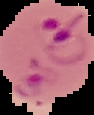
preparation = thin blood smear
image size = 94×115 pixels
malaria status = parasitized
image type = cell region segmented out of the field of view; surrounding area masked to black